Identify the cell.
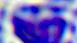

A leukocyte.

Summary:
  - Magnification: 400x
  - Modality: micrograph